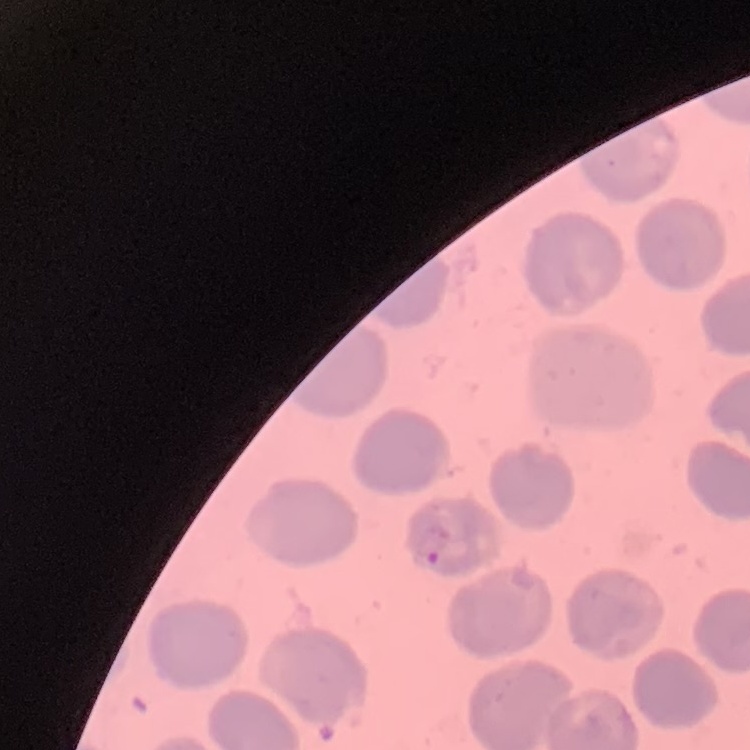
The red blood cells exhibit no rouleaux formation. Square crop of a larger photomicrograph. Thin blood smear. Field's or Giemsa stain.